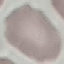

malaria status = uninfected
capture = smartphone through the microscope eyepiece
stain = Giemsa
image type = automatically extracted cell patch, resized to 64 × 64 pixels
preparation = thin blood smear